Point out each Plasmodium parasite.
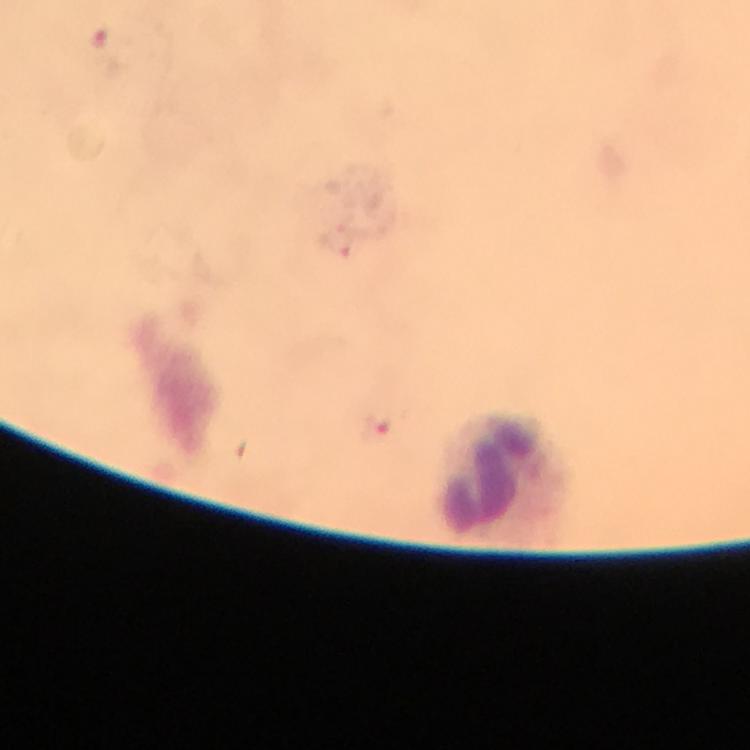
Approximate centers as {x, y} in pixels.
Plasmodium parasites: {100, 36}, {337, 242}, {375, 428}.

magnification = 100x
context = from a malaria diagnostic workup
capture = smartphone camera through the microscope
immersion oil = used
leukocyte locations = approximate centers as {x, y} in pixels: {504, 477}
image size = 750×750 pixels
cropped from = a single field of view
stain = Giemsa
preparation = thick smear